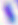

modality: photomicrograph
identification: Toxoplasma gondii
magnification: 400x